Give the preparation type.
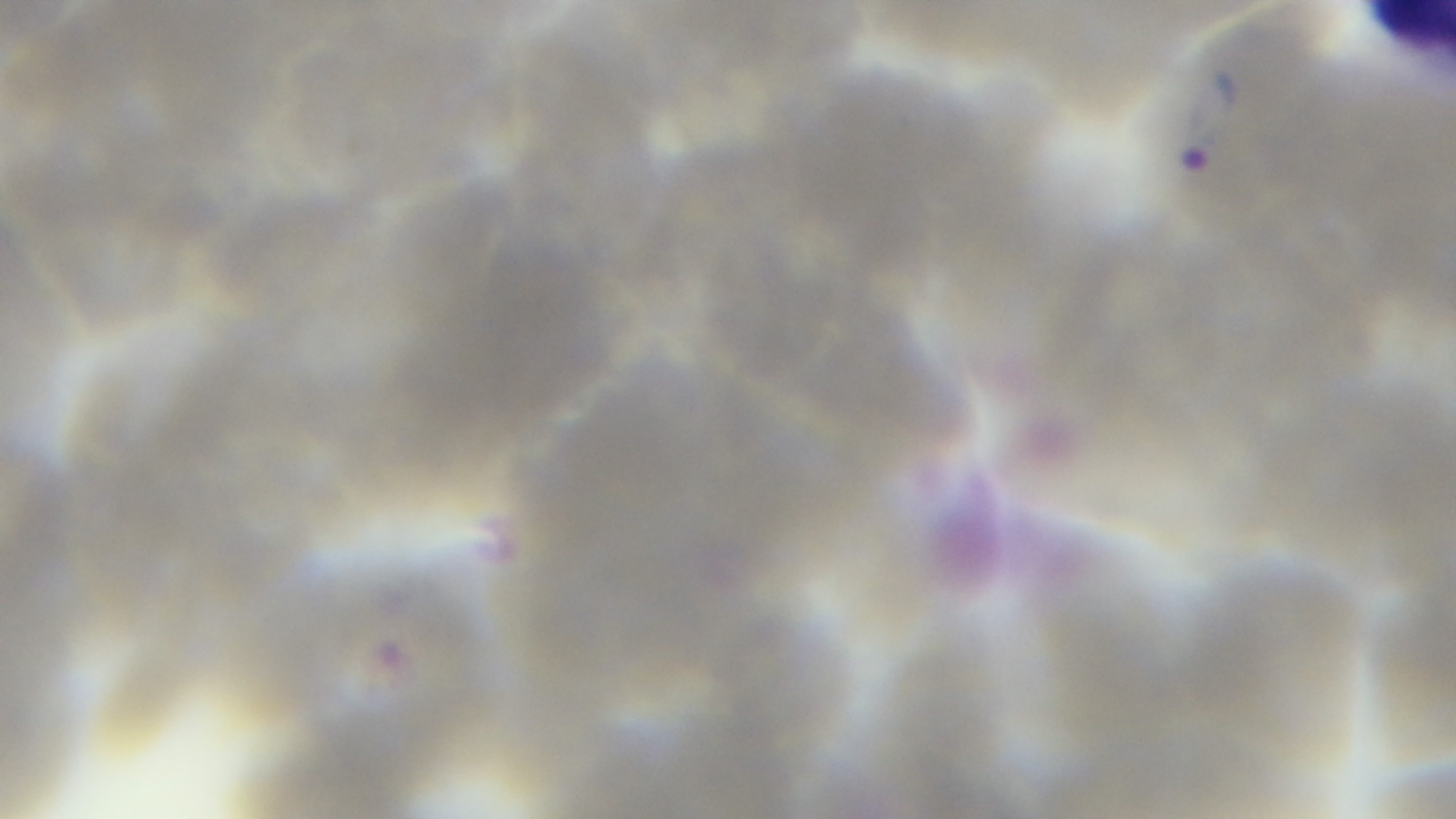
It is a thin blood film.

Captured with a mounted 4K digital camera. Giemsa stain. Oil-immersion objective, 100x. One field from the slide. Malaria status: positive. Light microscopy.